Give the position of every leukocyte visible.
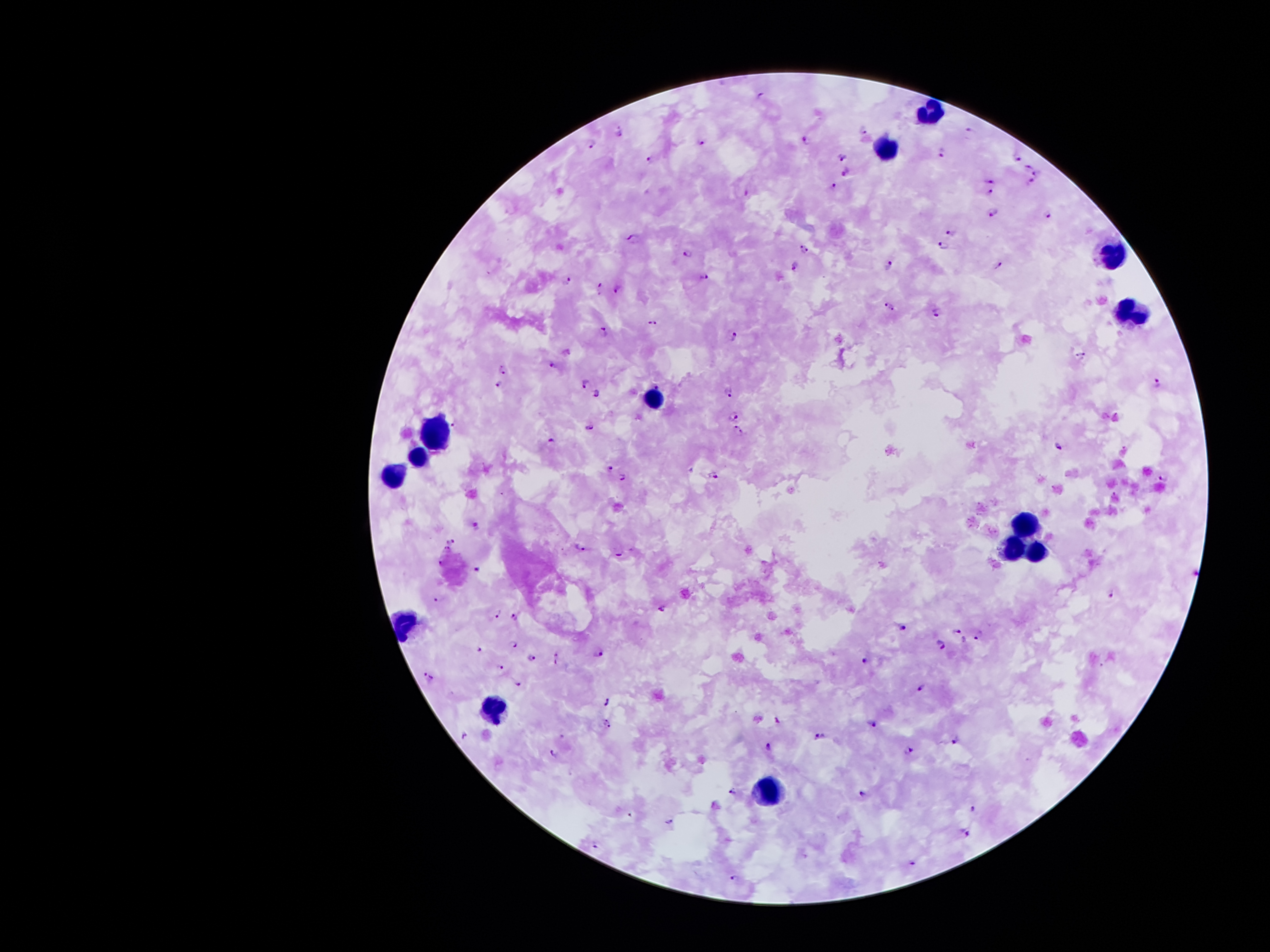

Approximate object centers, in pixels from the top-left corner.
Leukocytes: (x=928, y=109), (x=889, y=151), (x=1115, y=253), (x=1128, y=313), (x=435, y=434), (x=415, y=456), (x=394, y=477), (x=1026, y=518), (x=1016, y=549), (x=1041, y=553), (x=495, y=707), (x=772, y=792).

Plasmodium parasite locations: (x=763, y=94), (x=864, y=129), (x=618, y=131), (x=969, y=133), (x=702, y=140), (x=806, y=140), (x=591, y=142), (x=944, y=151), (x=1018, y=155), (x=840, y=156), (x=651, y=161), (x=1027, y=166), (x=846, y=173), (x=1037, y=173), (x=992, y=180), (x=1032, y=181), (x=834, y=185), (x=748, y=193), (x=991, y=193), (x=1049, y=212), (x=993, y=213), (x=951, y=232), (x=635, y=239), (x=943, y=245), (x=804, y=250), (x=688, y=253), (x=890, y=265), (x=795, y=266), (x=998, y=266), (x=705, y=278), (x=569, y=279), (x=601, y=288), (x=618, y=288), (x=890, y=306), (x=938, y=312), (x=652, y=323), (x=605, y=330), (x=736, y=336), (x=1080, y=356), (x=552, y=363), (x=505, y=367), (x=585, y=383), (x=1157, y=384), (x=501, y=385), (x=728, y=392), (x=596, y=393), (x=734, y=415), (x=454, y=424), (x=589, y=428), (x=739, y=432), (x=552, y=441), (x=1058, y=446), (x=610, y=469), (x=713, y=474), (x=623, y=477), (x=1165, y=477), (x=477, y=524), (x=451, y=540), (x=580, y=546), (x=447, y=548), (x=619, y=552), (x=441, y=562), (x=477, y=571), (x=1111, y=594), (x=438, y=599), (x=662, y=609), (x=498, y=613), (x=515, y=615), (x=901, y=627), (x=958, y=633), (x=978, y=634), (x=513, y=643), (x=941, y=645), (x=478, y=650), (x=599, y=652), (x=556, y=657), (x=532, y=658), (x=868, y=658), (x=501, y=666), (x=429, y=677), (x=518, y=682), (x=920, y=690), (x=608, y=700), (x=778, y=719), (x=874, y=724), (x=608, y=725), (x=821, y=737), (x=958, y=740), (x=770, y=746), (x=909, y=751), (x=555, y=752), (x=733, y=792), (x=864, y=794), (x=974, y=808), (x=631, y=814), (x=669, y=822), (x=965, y=833), (x=596, y=843), (x=912, y=863), (x=735, y=877). Single field of view. Giemsa stain. Thick peripheral-blood smear. Image is 1270×952 pixels. Patient malaria status: positive for Plasmodium falciparum. Photographed through the microscope eyepiece with a smartphone camera. 100x magnification.